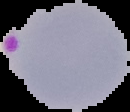
The area outside the segmented cell region is set to black. Image is 130×112 pixels. From a thin blood film. Malaria status: parasitized.